Classify this cell by malaria status.
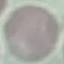
It is uninfected.

stain = Giemsa
image type = cell patch, automatically extracted from a larger field of view and resized to 64 × 64 pixels
capture = smartphone camera at the microscope eyepiece
preparation = thin blood film